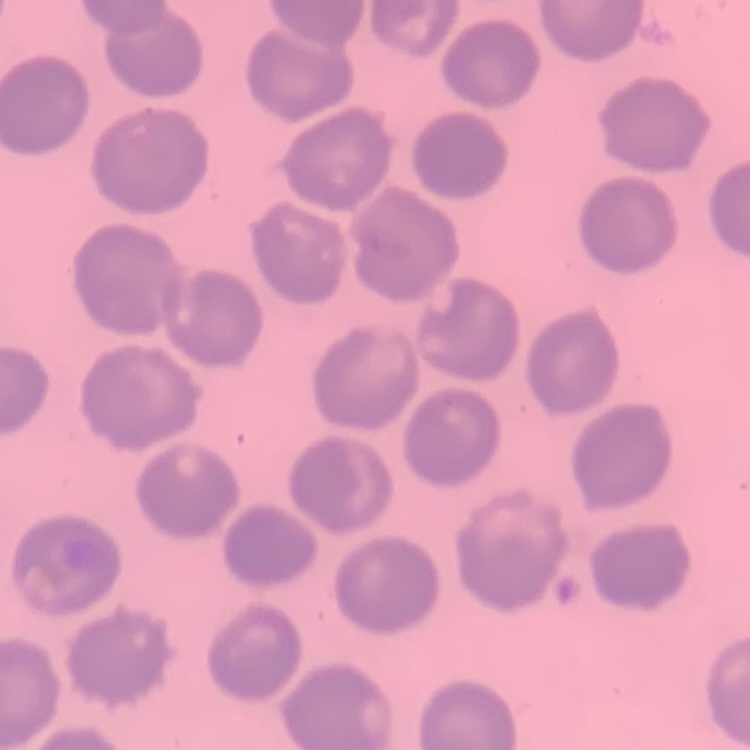 The red blood cells exhibit no rouleaux formation. Field's or Giemsa stain. Square crop of a larger photomicrograph. Thin peripheral smear.